State which parasite is depicted.
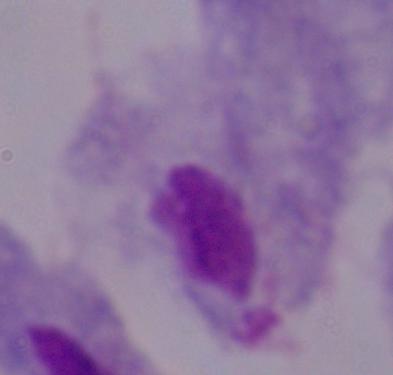
A trichomonad.

Summary:
  - Magnification: 1000x
  - Modality: micrograph